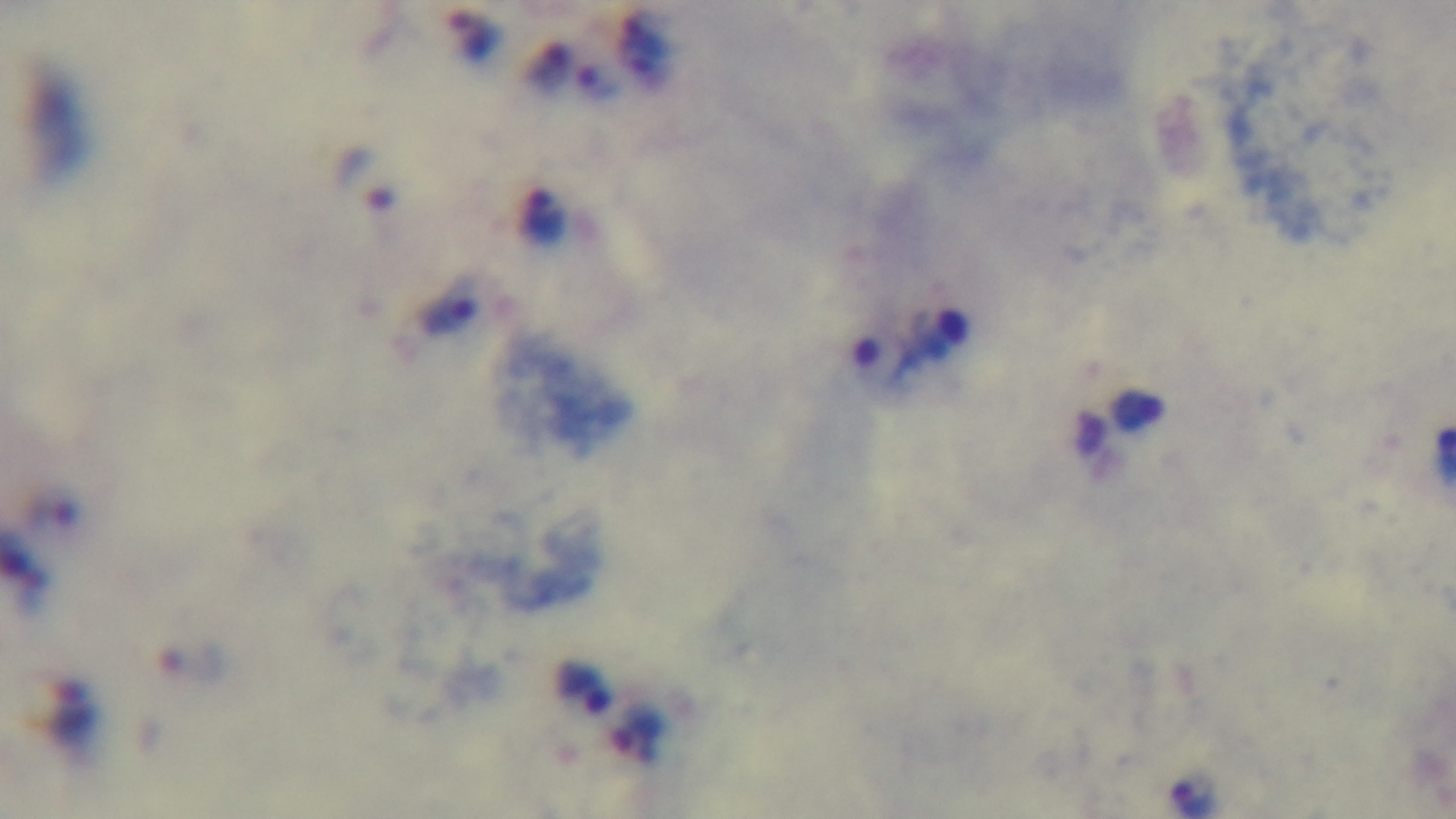
Summary:
  - Stain: Giemsa
  - Field of view: one from the slide
  - Modality: light microscopy
  - Preparation: thick
  - Malaria status: infected
  - Capture: mounted 4K digital camera
  - Objective: 100x oil immersion